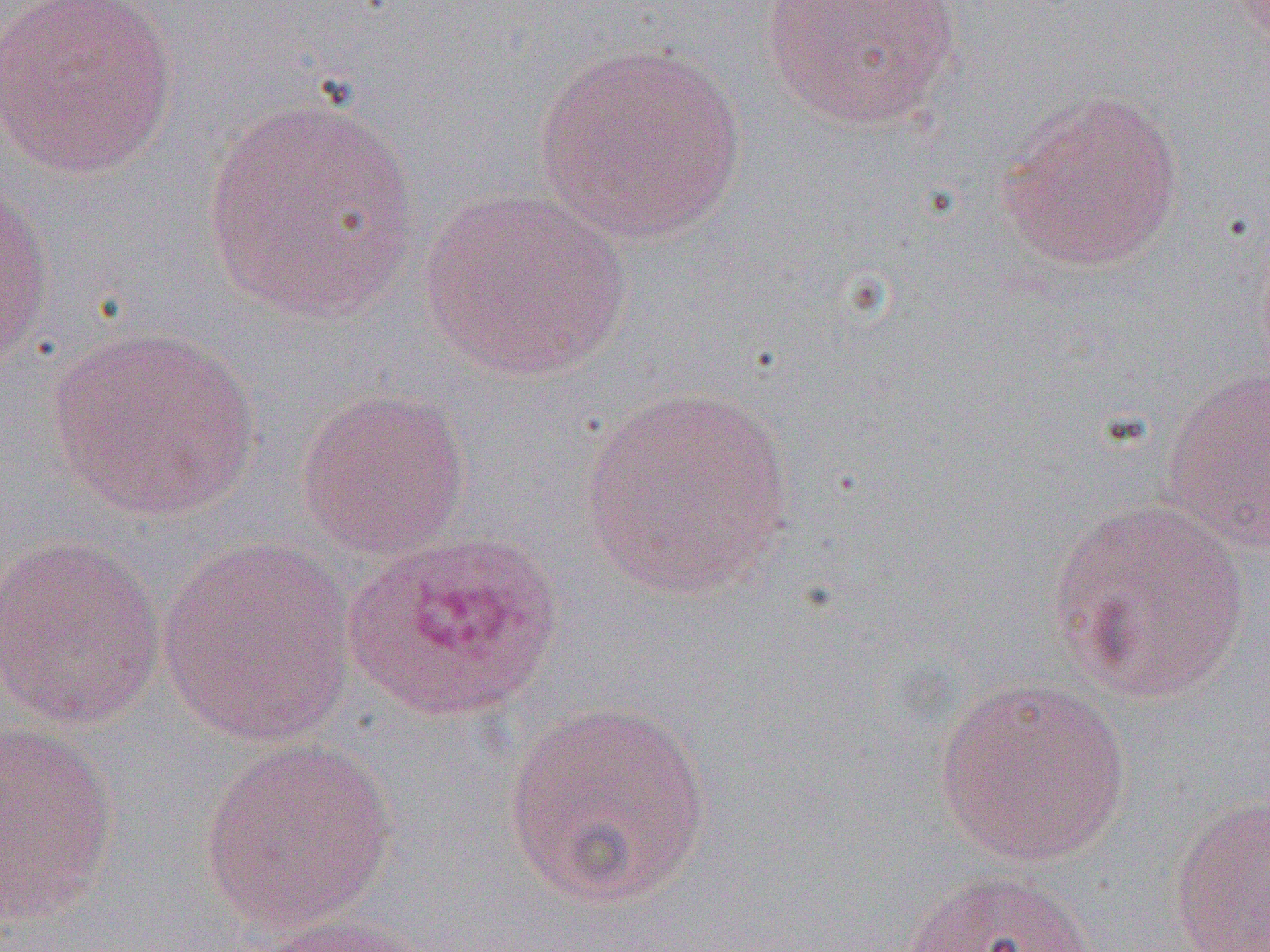
slide-level diagnosis = Plasmodium ovale
magnification = 1000x
uninfected red blood cell locations = approximate bounding boxes as (x1, y1, x2, y2) in pixels: (0, 0, 178, 179), (760, 0, 964, 131), (534, 40, 749, 245), (997, 90, 1185, 273), (202, 92, 423, 325), (0, 171, 56, 376), (415, 186, 635, 382), (48, 326, 260, 521), (1158, 364, 1270, 554), (578, 385, 797, 600), (295, 388, 471, 559), (1047, 497, 1252, 704), (0, 534, 168, 731), (156, 538, 359, 748), (933, 675, 1132, 867), (502, 699, 717, 909), (0, 721, 119, 925), (199, 735, 397, 934), (1168, 793, 1269, 952), (899, 867, 1100, 952), (241, 914, 437, 952)
Plasmodium ovale-infected red blood cell locations = approximate bounding boxes as (x1, y1, x2, y2) in pixels: (342, 529, 565, 725)
image size = 1270×952 pixels
modality = optical microscopy
field of view = one of a larger specimen
preparation = thin blood film